Assess this cell for malaria.
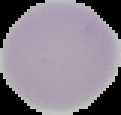

Uninfected.

Segmented cell region on a black background. From a thin blood film. Image is 121×115 pixels.